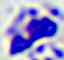 Micrograph. Captured at 400x magnification. A leukocyte is seen.